Describe the morphology of the erythrocytes.
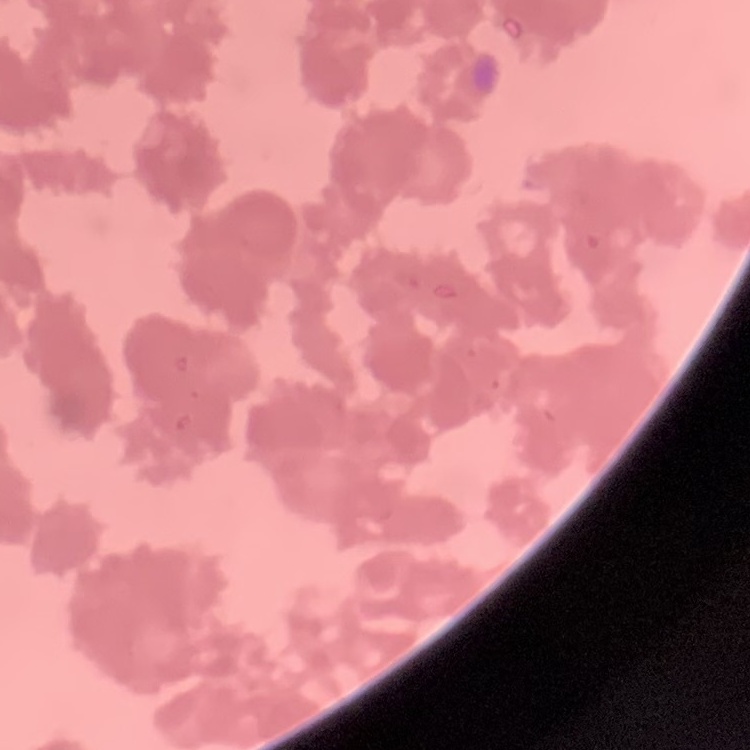

Rouleaux formation.

Summary:
  - Preparation: thin peripheral smear
  - Stain: Field's or Giemsa
  - Image type: square crop of a larger photomicrograph